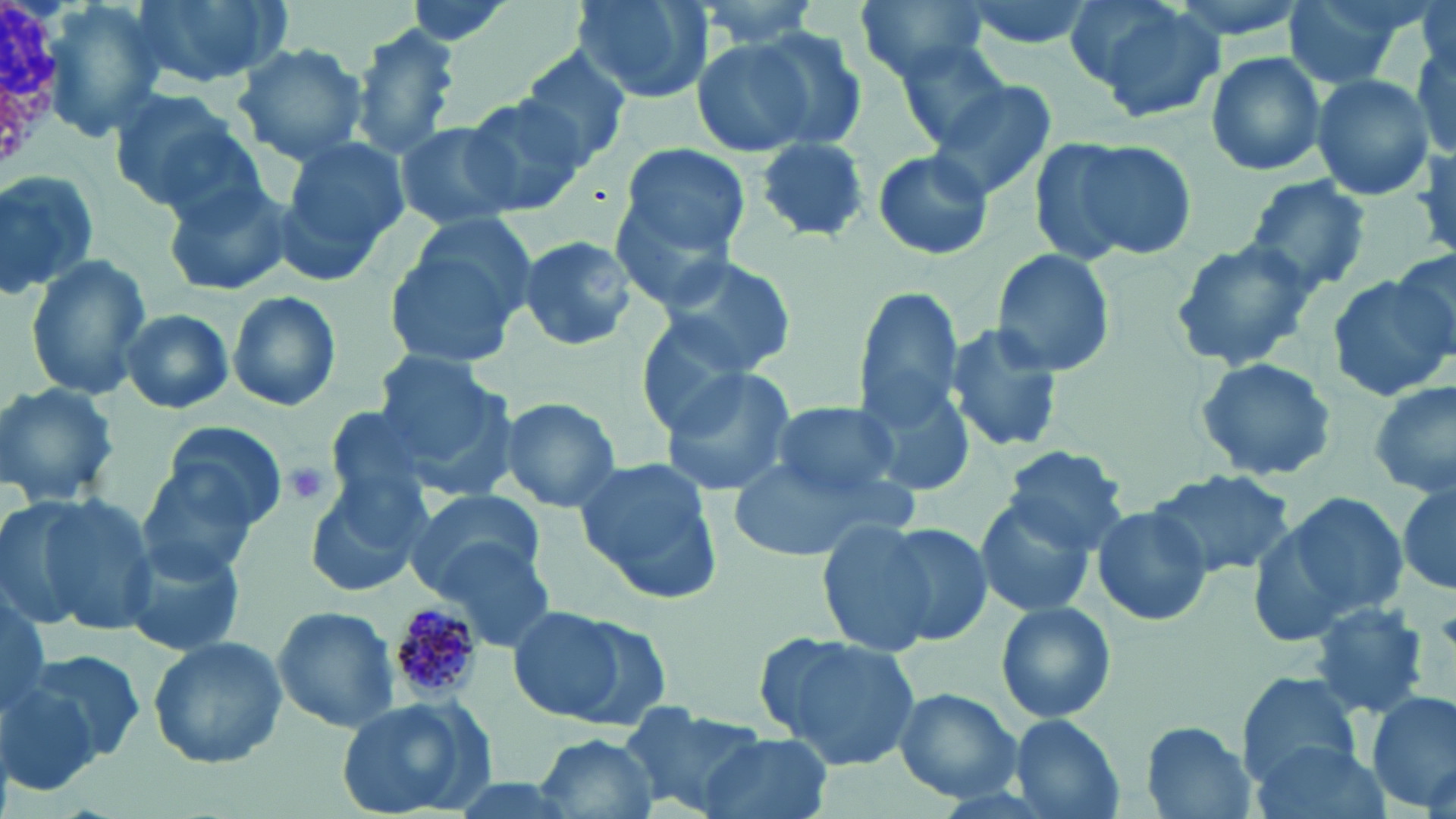

{
  "slide_level_diagnosis": "Plasmodium malariae",
  "white_blood_cell_locations": "approximate bounding boxes as (x1, y1, x2, y2) in pixels: (0, 0, 65, 166)",
  "plasmodium_malariae_infected_red_blood_cell_locations": "approximate bounding boxes as (x1, y1, x2, y2) in pixels: (389, 603, 484, 704)",
  "uninfected_red_blood_cell_locations": "approximate bounding boxes as (x1, y1, x2, y2) in pixels: (129, 0, 292, 87), (570, 0, 711, 104), (682, 0, 828, 49), (854, 0, 994, 83), (960, 0, 1098, 51), (1081, 0, 1226, 120), (1282, 0, 1417, 89), (38, 2, 167, 145), (354, 24, 459, 160), (739, 25, 869, 150), (1409, 28, 1455, 160), (687, 32, 825, 157), (895, 37, 1014, 150), (231, 41, 369, 164), (514, 47, 634, 169), (1205, 50, 1326, 176), (1312, 74, 1434, 202), (927, 76, 1058, 201), (106, 88, 257, 216), (461, 96, 589, 216), (392, 120, 525, 233), (1032, 134, 1196, 265), (754, 138, 873, 242), (279, 139, 406, 279), (618, 142, 751, 261), (1405, 147, 1456, 264), (872, 149, 994, 261), (0, 172, 97, 302), (1242, 175, 1372, 294), (161, 177, 294, 298), (611, 187, 746, 310), (384, 228, 535, 375), (513, 236, 640, 353), (1169, 237, 1316, 373), (990, 248, 1118, 378), (656, 250, 800, 375), (1390, 250, 1455, 346), (23, 255, 151, 402), (1328, 273, 1456, 401), (853, 284, 969, 432), (226, 289, 341, 413), (118, 308, 235, 413), (635, 320, 766, 444), (945, 320, 1064, 455), (371, 351, 510, 473), (1195, 354, 1337, 483), (658, 366, 800, 499), (853, 367, 981, 500), (1369, 379, 1455, 499), (0, 381, 119, 507), (497, 396, 622, 513), (760, 401, 909, 501), (320, 405, 437, 513), (159, 420, 286, 532), (1002, 445, 1135, 553), (721, 452, 905, 564), (573, 454, 729, 606), (132, 465, 263, 584), (1148, 469, 1294, 578), (303, 477, 427, 599), (1395, 484, 1455, 596), (403, 487, 545, 597), (1258, 488, 1413, 641), (11, 492, 156, 636), (973, 497, 1100, 619), (1091, 505, 1214, 628), (815, 522, 940, 655), (873, 524, 994, 647), (115, 539, 246, 655), (431, 539, 557, 653), (0, 590, 51, 719), (992, 600, 1118, 724), (1308, 603, 1429, 719), (271, 605, 400, 733), (507, 608, 636, 723), (555, 617, 676, 733), (755, 631, 923, 771), (147, 635, 288, 768), (13, 650, 144, 773), (1238, 671, 1362, 783), (893, 689, 1022, 801), (1367, 690, 1455, 815), (331, 697, 495, 814), (620, 706, 771, 816), (1008, 715, 1126, 819), (1140, 722, 1255, 818), (531, 731, 661, 819), (697, 733, 834, 819), (1247, 739, 1390, 819), (437, 776, 597, 819)",
  "magnification": "1000x",
  "modality": "light microscopy",
  "image_size": "1456×819 pixels",
  "preparation": "thin blood film",
  "stain": "May-Grünwald-Giemsa",
  "field_of_view": "single",
  "platelet_locations": "approximate bounding boxes as (x1, y1, x2, y2) in pixels: (285, 462, 330, 507)"
}